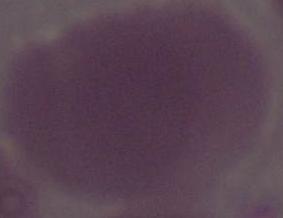

Micrograph. An erythrocyte is seen. Captured at 1000x magnification.